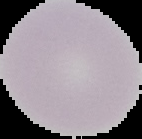

image type = segmented cell region with the area outside set to black
preparation = thin blood smear
image size = 142×139 pixels
malaria status = uninfected